Identify the parasite.
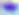

This is Toxoplasma gondii.

Summary:
  - Magnification: 400x
  - Modality: micrograph